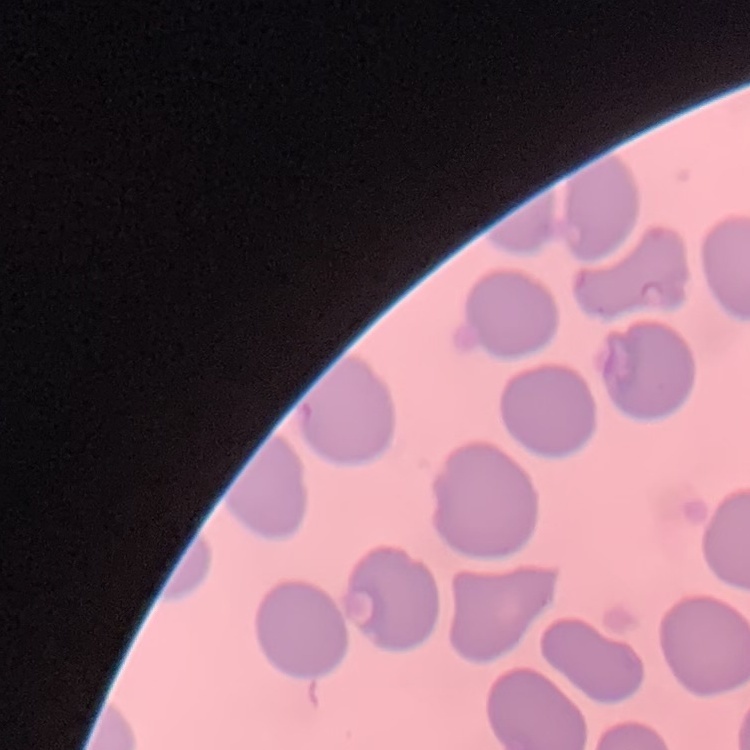

Summary:
  - Red blood cell morphology: no rouleaux formation
  - Image type: one tile cut from a larger photomicrograph
  - Stain: Field's or Giemsa
  - Preparation: thin blood film